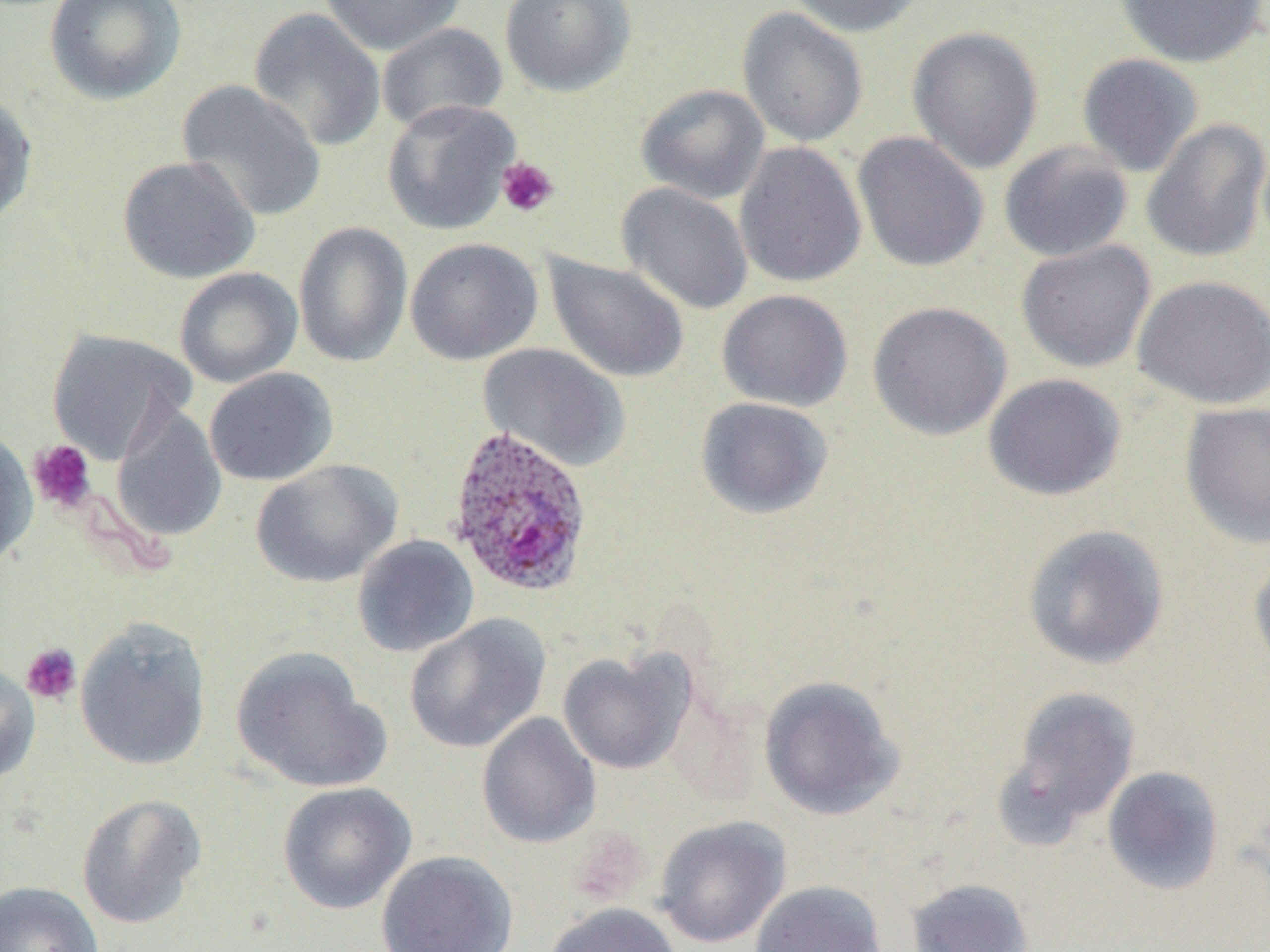

Summary:
  - Coordinate format: approximate bounding boxes as (x1, y1, x2, y2) in pixels
  - Uninfected red blood cell locations: (44, 0, 186, 106), (320, 0, 466, 55), (500, 0, 636, 97), (785, 0, 927, 38), (1114, 0, 1269, 68), (248, 7, 386, 154), (737, 7, 869, 148), (376, 22, 508, 135), (906, 25, 1044, 174), (1076, 53, 1204, 177), (176, 79, 326, 222), (635, 84, 770, 205), (0, 90, 39, 229), (381, 99, 520, 235), (1141, 119, 1270, 262), (852, 131, 989, 273), (998, 141, 1134, 263), (734, 142, 867, 288), (117, 155, 261, 284), (617, 183, 753, 315), (292, 221, 413, 368), (405, 237, 543, 366), (1015, 240, 1156, 373), (543, 253, 690, 384), (173, 266, 303, 387), (1131, 274, 1270, 410), (717, 289, 853, 411), (867, 300, 1013, 441), (44, 328, 195, 463), (479, 343, 630, 472), (204, 367, 339, 487), (983, 373, 1126, 501), (695, 396, 834, 520), (1180, 401, 1270, 548), (111, 403, 227, 542), (0, 426, 37, 572), (250, 458, 402, 588), (1021, 523, 1170, 671), (352, 534, 479, 657), (1248, 548, 1270, 676), (404, 615, 551, 754), (74, 616, 213, 771), (230, 648, 390, 793), (557, 650, 693, 774), (0, 660, 41, 785), (759, 675, 904, 820), (1001, 685, 1141, 837), (476, 713, 602, 849), (1101, 765, 1226, 894), (277, 782, 416, 914), (76, 793, 207, 930), (654, 815, 791, 948), (376, 850, 519, 952), (906, 877, 1035, 952), (0, 880, 104, 952), (749, 880, 887, 952), (542, 902, 682, 952)
  - Plasmodium ovale-infected red blood cell locations: (446, 425, 594, 598)
  - Platelet locations: (496, 156, 559, 218), (27, 439, 97, 514), (21, 642, 82, 705)
  - Slide-level diagnosis: Plasmodium ovale
  - Preparation: thin blood smear
  - Stain: May-Grünwald-Giemsa
  - Magnification: 1000x
  - Image size: 1270×952 pixels
  - Field of view: single
  - Modality: light microscopy